Name the parasite shown.
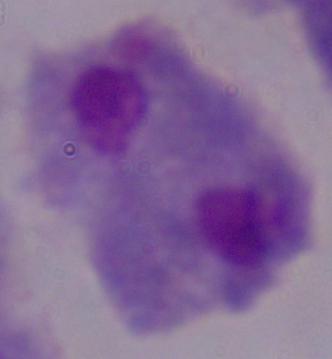

A trichomonad.

1000x magnification. Photomicrograph.